State which cell type is depicted.
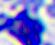
A leukocyte.

Summary:
  - Modality: micrograph
  - Magnification: 400x